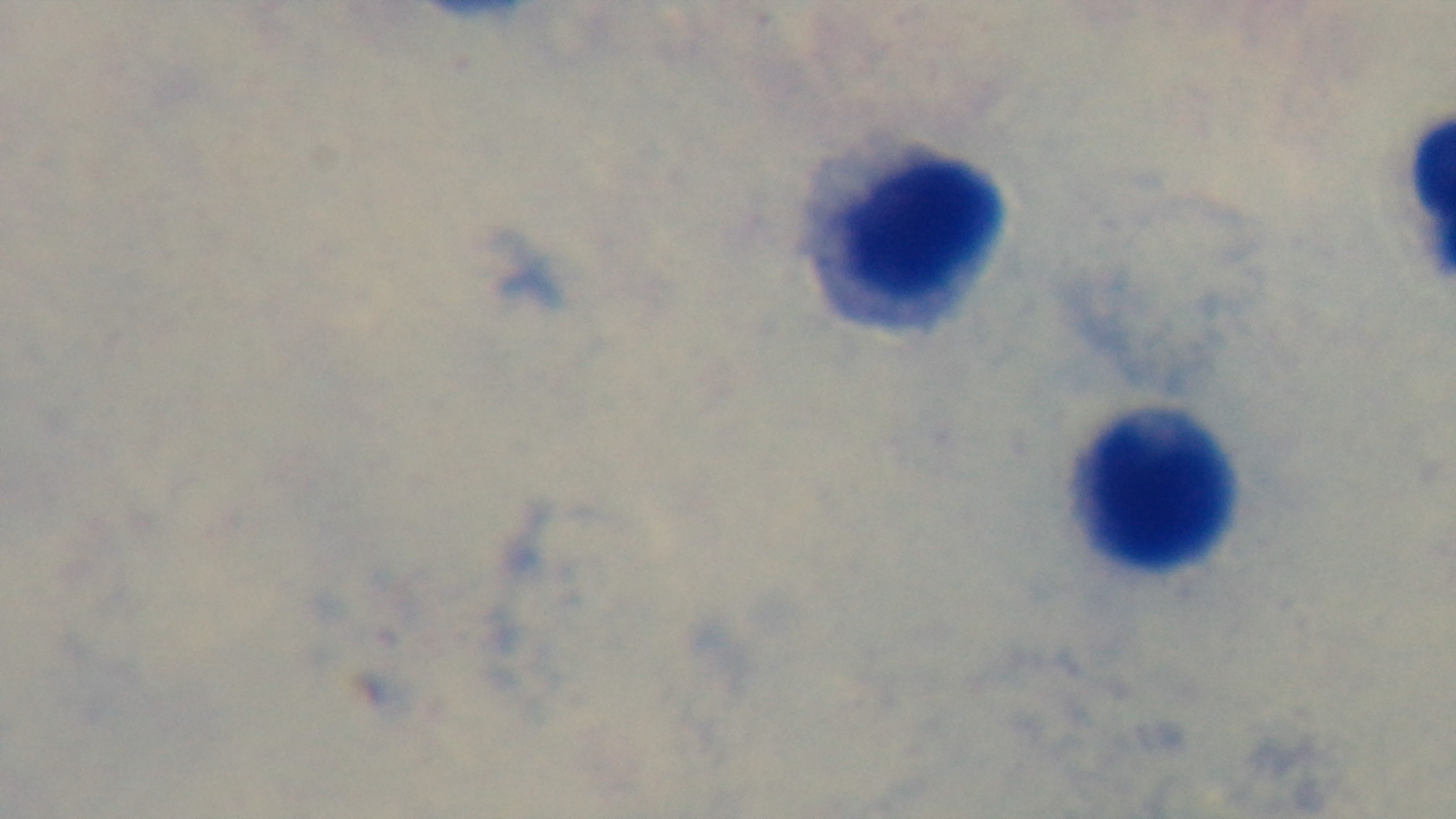

Preparation: thick blood film. One field from the slide. Captured with a mounted 4K digital camera. Malaria status: negative. 100x oil-immersion objective. Giemsa-stained. Photomicrograph.